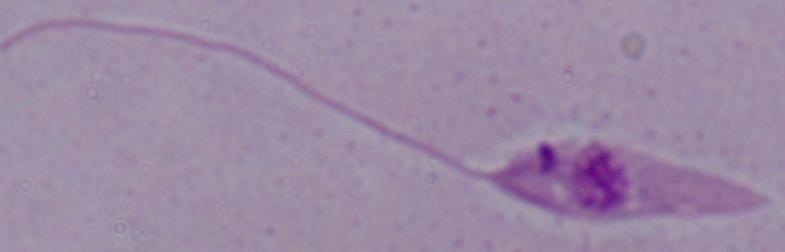

1000x magnification. Photomicrograph. A Leishmania parasite is seen.